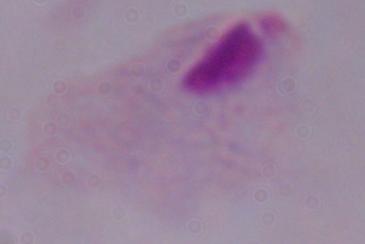

{
  "identification": "trichomonad",
  "modality": "micrograph",
  "magnification": "1000x"
}